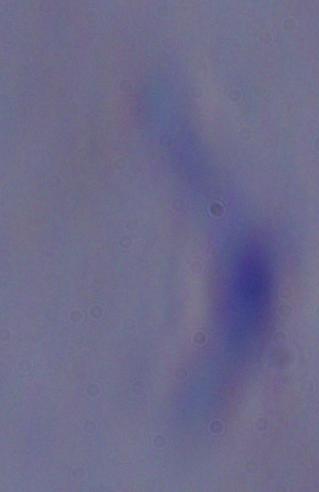

{
  "identification": "trypanosome",
  "modality": "micrograph",
  "magnification": "1000x"
}